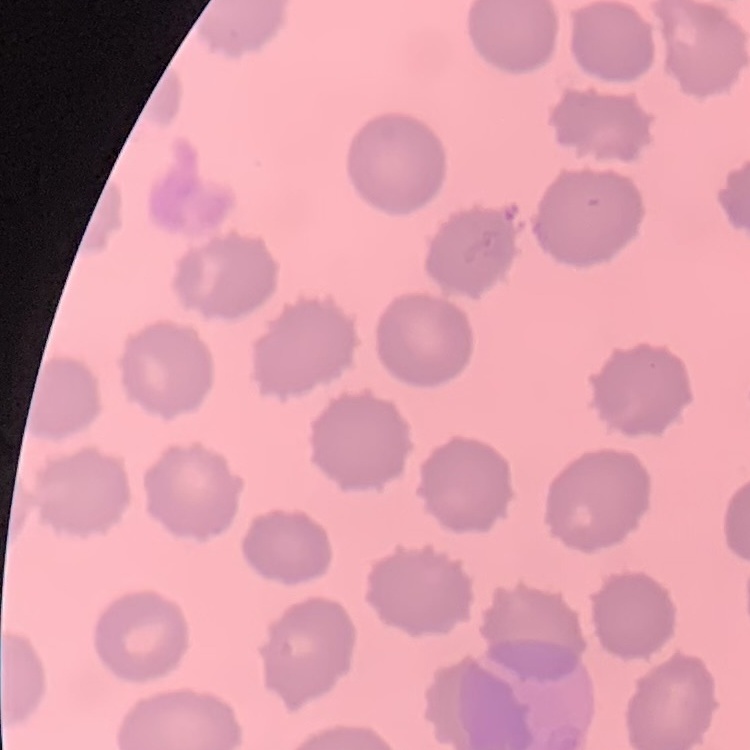
red_blood_cell_morphology: no rouleaux formation
image_type: one tile cut from a larger photomicrograph
stain: Field's or Giemsa
preparation: thin blood film